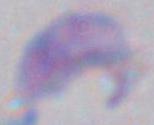

Summary:
  - Modality: photomicrograph
  - Identification: Toxoplasma gondii
  - Magnification: 1000x